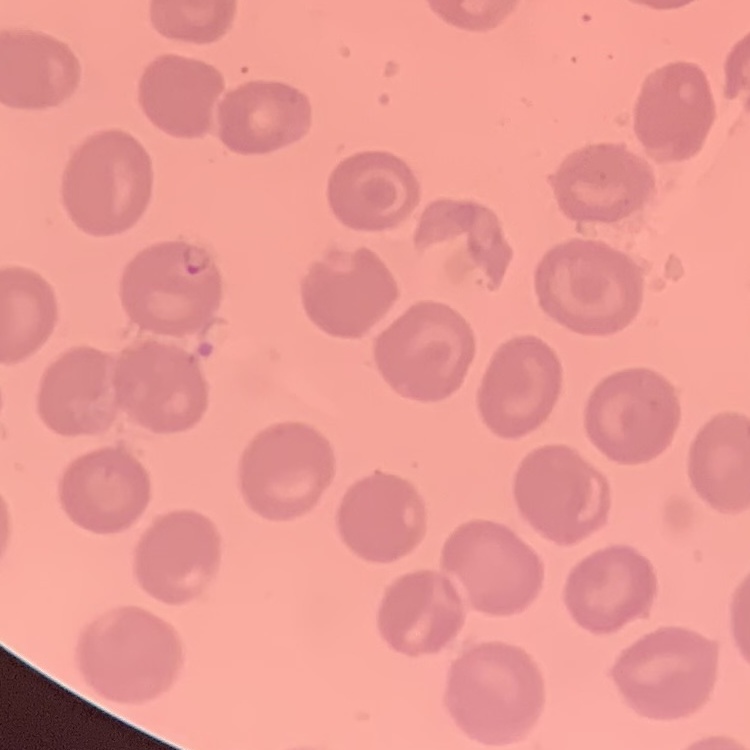

Summary:
  - Red blood cell morphology: no rouleaux formation
  - Image type: one tile cut from a larger photomicrograph
  - Preparation: thin blood film
  - Stain: Field's or Giemsa